Identify the parasite.
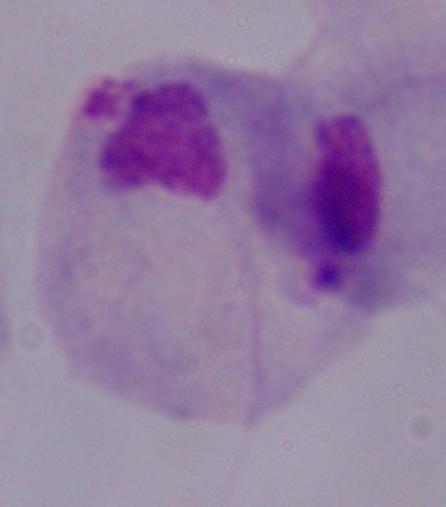
This is a trichomonad.

Micrograph. Captured at 1000x magnification.